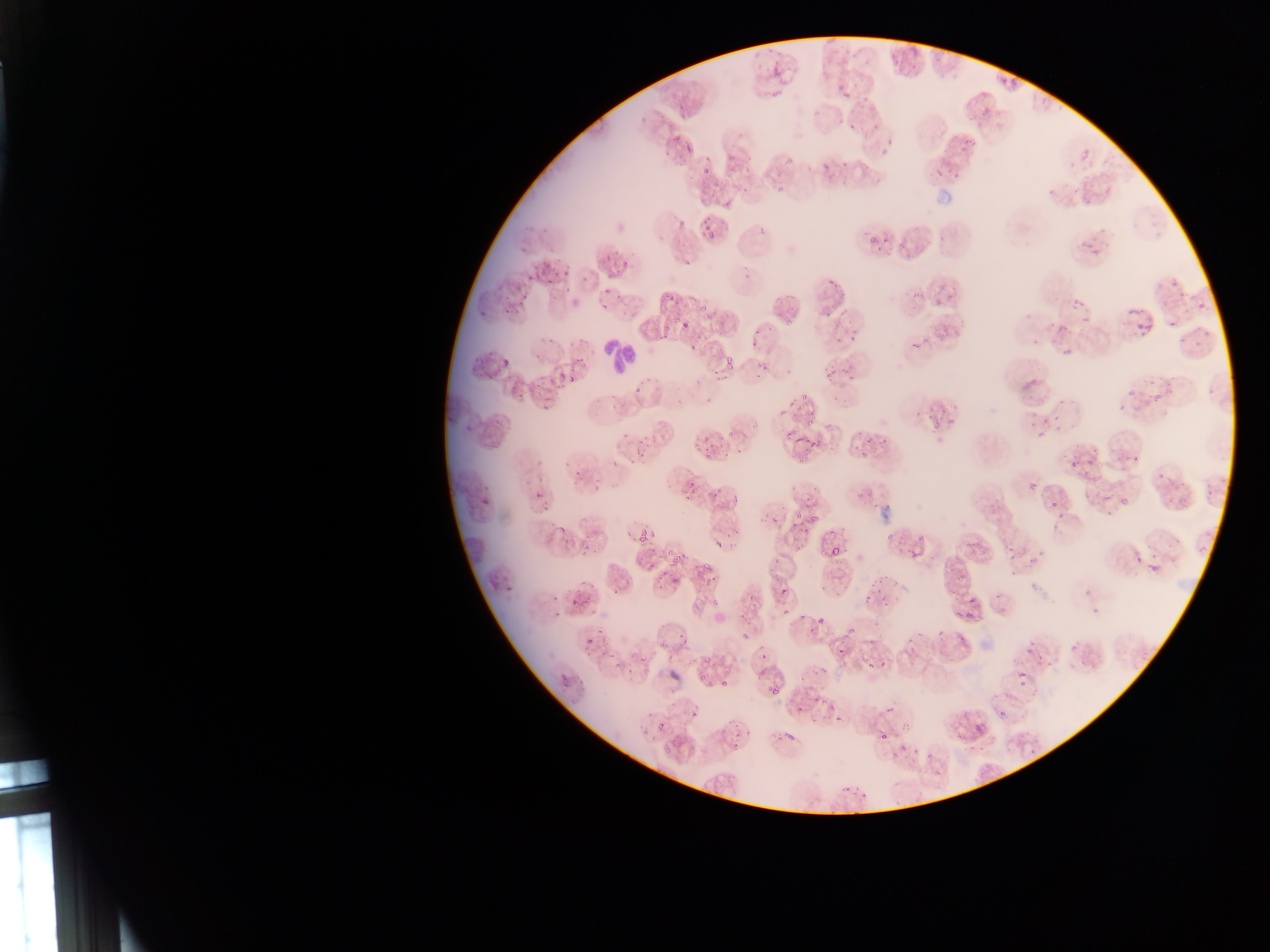
{
  "leukocyte_locations": "approximate bounding boxes as (left, top, right, bottom) in pixels: (592, 336, 637, 379)",
  "field_of_view": "single",
  "image_size": "1270×952 pixels",
  "capture": "mobile-phone photograph through a microscope",
  "preparation": "thin blood smear",
  "country": "Ghana",
  "malaria_parasite_locations": "approximate bounding boxes as (left, top, right, bottom) in pixels: (891, 56, 901, 62), (771, 65, 782, 79), (907, 68, 919, 77), (1005, 80, 1016, 88), (769, 85, 781, 97), (838, 91, 850, 99), (978, 103, 993, 115), (676, 105, 685, 112), (868, 121, 879, 128), (848, 122, 857, 130), (672, 133, 680, 143), (878, 138, 895, 159), (679, 139, 697, 161), (727, 153, 737, 164), (786, 157, 794, 165), (699, 158, 713, 177), (823, 163, 831, 168), (951, 168, 964, 180), (773, 169, 785, 179), (931, 169, 941, 177), (774, 183, 791, 194), (1047, 187, 1059, 197), (1083, 196, 1096, 203), (702, 224, 720, 240), (865, 237, 883, 248), (1079, 238, 1095, 248), (517, 242, 530, 254), (1089, 251, 1104, 259), (612, 258, 632, 277), (683, 258, 692, 266), (529, 265, 540, 274), (563, 266, 572, 274), (742, 270, 754, 279), (526, 273, 533, 281), (547, 273, 556, 284), (828, 275, 838, 290), (1169, 279, 1181, 294), (513, 280, 525, 291), (601, 285, 614, 295), (560, 286, 569, 293), (661, 290, 676, 309), (786, 291, 797, 303), (1070, 296, 1086, 308), (518, 299, 529, 306), (1194, 302, 1205, 312), (697, 304, 713, 313), (600, 305, 609, 311), (479, 309, 489, 316), (1126, 309, 1138, 315), (703, 313, 711, 322), (820, 313, 834, 321), (1081, 314, 1091, 323), (1166, 316, 1181, 327), (672, 318, 680, 327), (1056, 318, 1073, 330), (785, 319, 796, 326), (1136, 319, 1152, 330), (680, 320, 690, 330), (835, 321, 845, 331), (849, 327, 860, 341), (752, 329, 763, 336), (1197, 330, 1211, 337), (834, 333, 844, 345), (658, 335, 668, 344), (746, 337, 757, 348), (921, 337, 931, 344), (1177, 338, 1189, 346), (1194, 339, 1204, 345), (687, 340, 701, 349), (909, 342, 921, 351), (1060, 345, 1076, 360), (823, 355, 838, 379), (498, 357, 514, 369), (721, 359, 733, 371), (848, 359, 861, 376), (752, 363, 764, 376), (557, 367, 566, 379), (707, 367, 719, 377), (565, 372, 575, 386), (1020, 378, 1041, 392), (634, 384, 643, 394), (534, 386, 542, 398), (1205, 387, 1215, 398), (1124, 388, 1148, 394), (516, 391, 523, 402), (796, 395, 807, 407), (1119, 395, 1130, 413), (1152, 395, 1159, 403), (784, 398, 794, 412), (803, 417, 816, 428), (464, 420, 475, 431), (932, 420, 941, 428), (1035, 428, 1052, 442), (726, 429, 735, 441), (880, 434, 891, 446), (863, 435, 871, 445), (482, 436, 504, 449), (694, 437, 715, 456), (794, 437, 803, 444), (808, 437, 821, 447), (635, 444, 645, 459), (795, 452, 807, 468), (1125, 452, 1143, 460), (611, 455, 622, 466), (1066, 455, 1083, 475), (573, 470, 581, 477), (1156, 473, 1167, 481), (1172, 481, 1185, 487), (681, 484, 696, 503), (1206, 488, 1216, 501), (533, 489, 542, 500), (479, 491, 489, 506), (724, 493, 741, 508), (1050, 498, 1059, 511), (1117, 498, 1128, 507), (792, 505, 805, 533), (806, 506, 817, 533), (1055, 508, 1071, 522), (770, 512, 779, 526), (636, 524, 651, 546), (556, 527, 564, 538), (714, 536, 722, 549), (1007, 541, 1016, 553), (832, 543, 845, 557), (794, 545, 802, 554), (673, 555, 683, 564), (701, 555, 714, 567), (1029, 555, 1039, 569), (1148, 560, 1159, 573), (958, 568, 971, 583), (705, 574, 717, 589), (671, 577, 680, 586), (770, 582, 798, 605), (612, 590, 622, 596), (1080, 592, 1109, 617), (572, 593, 584, 609), (809, 606, 837, 629), (794, 611, 813, 633), (730, 623, 761, 650), (582, 630, 602, 648), (679, 632, 687, 644), (657, 638, 670, 653), (1023, 639, 1040, 664), (835, 646, 849, 658), (701, 655, 713, 666), (840, 658, 851, 673), (864, 658, 875, 673), (759, 669, 767, 678), (1013, 671, 1031, 688), (663, 672, 683, 686), (717, 674, 733, 694), (699, 676, 710, 684), (771, 687, 779, 695), (817, 690, 834, 707), (657, 721, 665, 731), (973, 722, 984, 733), (775, 726, 798, 744), (874, 727, 889, 741), (953, 731, 964, 745), (661, 739, 680, 754), (890, 742, 909, 756), (1027, 747, 1035, 754), (923, 752, 935, 760), (856, 792, 868, 807) | approximate (x, y) pixel centers of objects too small to bound: (508, 311), (890, 537), (971, 600), (1002, 713)"
}